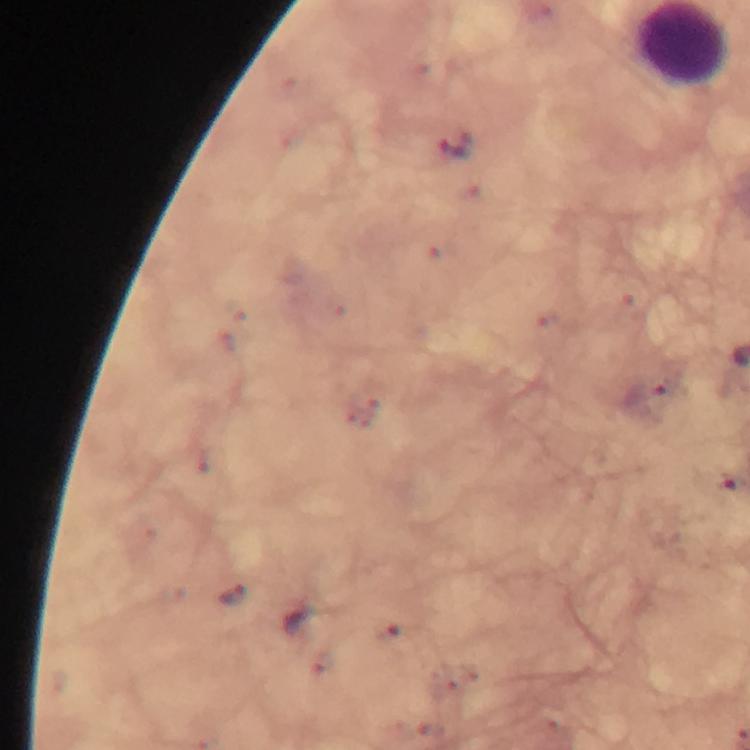
Approximate centers as {x, y} in pixels. Malaria parasite locations: {454, 149}, {236, 594}. Thick blood film. A crop from one field of view. Image is 750×750 pixels. Giemsa-stained preparation. Smartphone photograph taken through a microscope. Immersion oil was used. From a malaria diagnostic workup. 100x magnification.